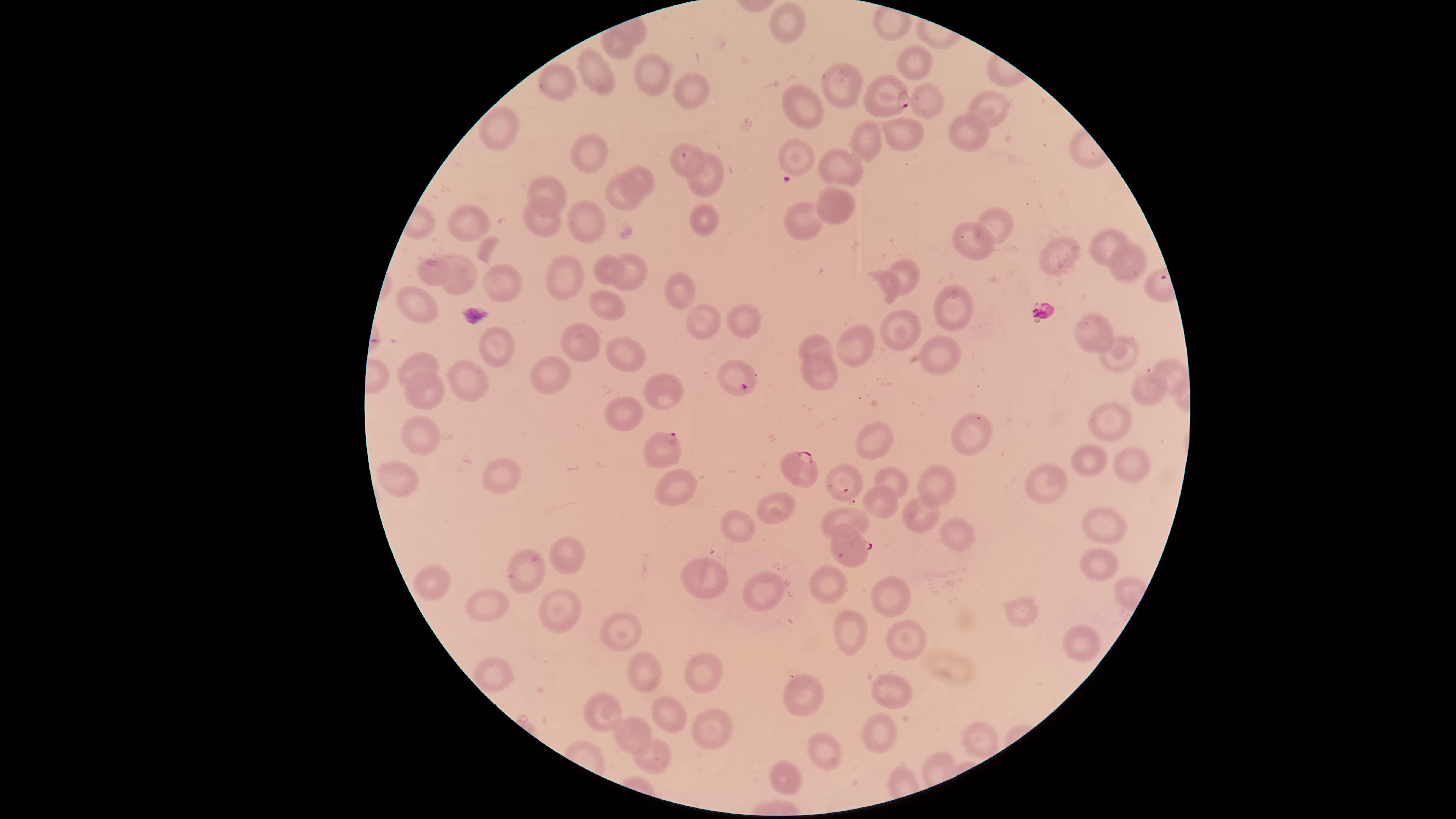
Approximate marker points as {x, y} in pixels. Uninfected red blood cells: {793, 24}, {619, 44}, {912, 58}, {594, 73}, {656, 73}, {555, 80}, {845, 83}, {695, 87}, {919, 102}, {806, 106}, {989, 109}, {499, 131}, {901, 131}, {968, 134}, {795, 148}, {593, 152}, {687, 155}, {840, 167}, {644, 176}, {712, 180}, {550, 184}, {835, 198}, {620, 200}, {696, 217}, {594, 218}, {475, 220}, {543, 220}, {993, 227}, {802, 228}, {972, 239}, {1109, 240}, {1059, 258}, {608, 263}, {431, 269}, {910, 270}, {1126, 271}, {570, 272}, {625, 272}, {463, 280}, {883, 282}, {505, 283}, {679, 287}, {420, 301}, {608, 311}, {948, 311}, {701, 323}, {911, 326}, {1099, 327}, {741, 328}, {586, 341}, {816, 344}, {858, 345}, {498, 349}, {1124, 349}, {622, 351}, {936, 354}, {426, 361}, {1170, 373}, {817, 378}, {551, 379}, {470, 385}, {1143, 390}, {668, 392}, {426, 395}, {623, 419}, {1108, 425}, {971, 437}, {419, 438}, {876, 440}, {1090, 459}, {1122, 468}, {939, 473}, {841, 474}, {506, 475}, {888, 475}, {1047, 477}, {404, 478}, {682, 485}, {884, 504}, {777, 506}, {845, 519}, {923, 519}, {741, 523}, {1094, 528}, {959, 529}, {570, 553}, {529, 566}, {1090, 567}, {705, 575}, {828, 582}, {442, 586}, {766, 591}, {896, 601}, {494, 603}, {1015, 612}, {559, 614}, {624, 629}, {855, 634}, {906, 639}, {1077, 647}, {704, 667}, {646, 673}, {493, 677}, {892, 693}, {810, 702}, {603, 706}, {666, 713}, {635, 728}, {710, 732}, {878, 736}, {975, 736}, {833, 754}, {660, 765}, {788, 778}. Parasitized red blood cells: {890, 96}, {738, 376}, {667, 452}, {799, 468}, {850, 548}. Presence: malaria parasites identified. The visible region is circular. Giemsa-stained preparation. Smartphone photograph through the microscope eyepiece. One field of view of the specimen. Image is 1456×819 pixels. Thin blood film. Species: Plasmodium falciparum.